Locate and identify every blood parasite.
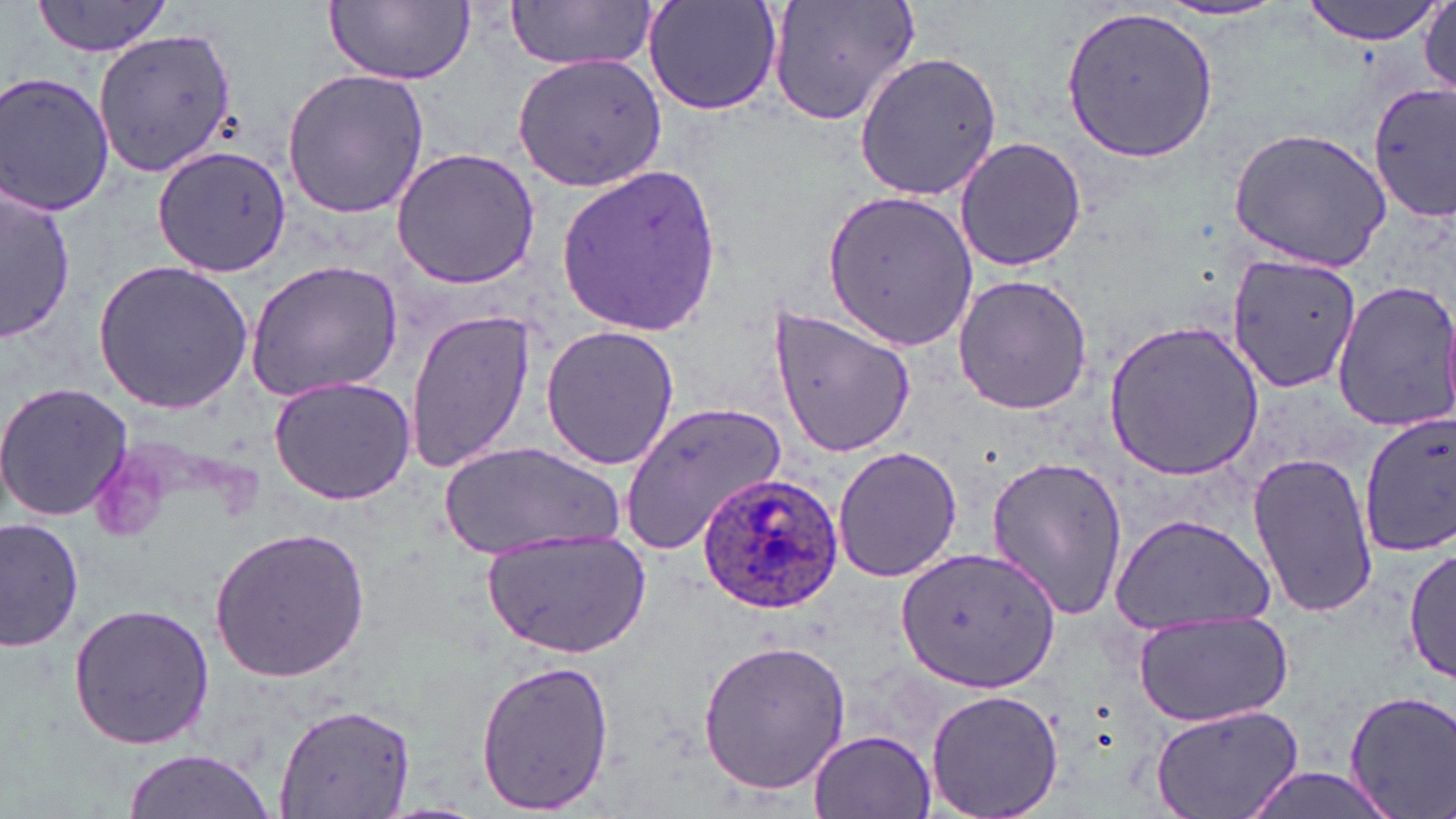
Approximate bounding boxes as [x1, y1, x2, y2] in pixels.
Plasmodium ovale-infected red blood cells: [697, 475, 846, 616].
No Plasmodium falciparum, Plasmodium malariae, Plasmodium vivax, Babesia divergens, or Trypanosoma brucei observed.

Uninfected red blood cell locations: [33, 0, 173, 60], [643, 0, 787, 116], [762, 0, 922, 125], [1299, 0, 1442, 43], [325, 1, 475, 85], [506, 1, 660, 73], [1061, 2, 1220, 163], [1158, 2, 1289, 24], [1418, 2, 1455, 101], [97, 29, 238, 175], [853, 52, 1004, 200], [511, 53, 667, 192], [280, 67, 432, 220], [0, 72, 116, 218], [1369, 83, 1456, 222], [1227, 126, 1392, 270], [954, 135, 1087, 272], [153, 143, 295, 277], [390, 148, 543, 290], [555, 162, 723, 339], [0, 178, 73, 346], [821, 187, 979, 352], [1227, 253, 1366, 393], [244, 258, 404, 402], [93, 260, 254, 416], [951, 275, 1095, 415], [1329, 279, 1456, 432], [768, 306, 914, 457], [405, 308, 535, 476], [1103, 319, 1264, 482], [540, 325, 682, 470], [266, 374, 417, 504], [0, 382, 133, 523], [622, 401, 787, 553], [1359, 412, 1456, 556], [439, 442, 626, 559], [831, 446, 963, 583], [1249, 450, 1380, 621], [986, 453, 1129, 621], [1108, 511, 1277, 634], [0, 516, 84, 653], [207, 525, 372, 683], [480, 532, 650, 658], [896, 545, 1061, 695], [1405, 546, 1455, 685], [66, 602, 216, 752], [1133, 611, 1294, 725], [697, 639, 850, 793], [475, 659, 616, 815], [923, 687, 1064, 819], [1342, 689, 1456, 819], [275, 700, 417, 818], [1148, 703, 1305, 819], [809, 729, 937, 819], [121, 749, 274, 817], [1234, 765, 1408, 819]. Slide-level diagnosis: Plasmodium ovale. Image is 1456×819 pixels. 1000x magnification. Thin blood smear. May-Grünwald-Giemsa-stained preparation. Single field of view. Light microscopy.